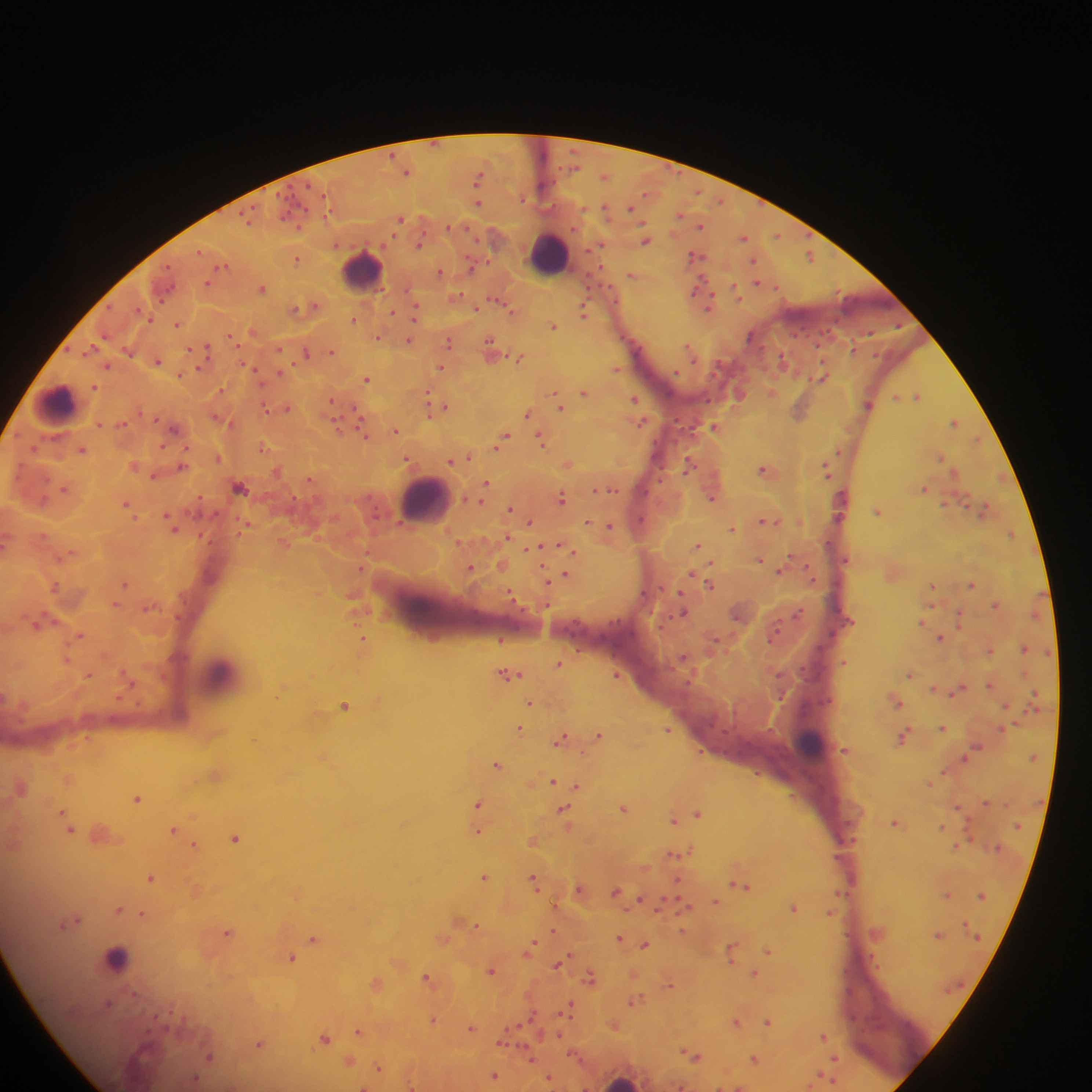
Approximate centers as [x, y] in pixels.
Summary:
  - Malaria parasite locations: [433, 143], [574, 151], [393, 153], [670, 166], [558, 167], [575, 168], [407, 171], [681, 174], [605, 176], [478, 179], [554, 179], [541, 183], [290, 186], [308, 186], [699, 192], [277, 194], [326, 197], [646, 197], [524, 201], [723, 201], [478, 202], [761, 202], [299, 204], [251, 207], [631, 208], [309, 209], [584, 209], [606, 210], [238, 213], [679, 215], [283, 216], [327, 216], [401, 218], [248, 222], [644, 223], [701, 225], [297, 226], [450, 227], [469, 228], [808, 233], [777, 235], [744, 237], [477, 238], [646, 240], [420, 243], [600, 245], [591, 252], [199, 253], [811, 255], [696, 256], [297, 259], [488, 261], [754, 261], [170, 265], [223, 266], [472, 267], [605, 267], [441, 271], [631, 275], [588, 277], [211, 281], [757, 283], [175, 285], [262, 288], [590, 288], [612, 288], [699, 291], [737, 293], [463, 295], [164, 300], [499, 300], [618, 302], [708, 305], [314, 306], [306, 307], [112, 308], [136, 308], [476, 308], [513, 310], [392, 311], [584, 311], [416, 313], [153, 319], [354, 319], [837, 322], [178, 324], [553, 326], [900, 326], [254, 331], [819, 331], [793, 333], [870, 334], [104, 336], [379, 336], [231, 337], [753, 337], [620, 338], [408, 341], [449, 341], [95, 344], [818, 347], [690, 348], [69, 349], [205, 349], [280, 349], [128, 350], [189, 350], [491, 350], [856, 350], [333, 351], [306, 352], [82, 355], [875, 355], [779, 356], [520, 358], [158, 361], [822, 361], [694, 362], [721, 363], [107, 366], [293, 366], [441, 367], [250, 368], [617, 368], [199, 369], [676, 371], [181, 374], [281, 374], [714, 374], [821, 375], [366, 379], [266, 384], [94, 385], [555, 391], [429, 392], [585, 392], [772, 392], [739, 393], [917, 396], [710, 397], [635, 398], [331, 400], [868, 404], [357, 406], [437, 406], [561, 406], [268, 408], [287, 408], [800, 410], [138, 412], [528, 414], [218, 418], [157, 419], [336, 419], [676, 420], [955, 421], [123, 423], [642, 423], [99, 424], [714, 426], [175, 428], [690, 428], [361, 429], [395, 430], [977, 438], [502, 440], [542, 440], [161, 445], [188, 445], [262, 447], [34, 450], [82, 450], [840, 451], [218, 457], [465, 457], [407, 458], [941, 458], [456, 459], [568, 463], [134, 464], [690, 464], [182, 465], [660, 469], [277, 470], [766, 470], [826, 470], [154, 476], [309, 479], [657, 480], [487, 484], [66, 487], [240, 488], [925, 488], [605, 489], [484, 490], [645, 490], [841, 492], [200, 497], [369, 497], [562, 497], [712, 497], [46, 499], [295, 499], [943, 504], [128, 505], [511, 508], [984, 509], [878, 511], [187, 512], [216, 514], [843, 516], [644, 519], [530, 521], [769, 521], [588, 522], [246, 525], [173, 526], [610, 526], [732, 529], [1012, 532], [203, 536], [507, 537], [830, 540], [6, 543], [284, 543], [459, 544], [698, 545], [537, 547], [567, 548], [573, 551], [370, 552], [66, 555], [789, 557], [760, 559], [845, 559], [711, 562], [502, 565], [471, 567], [361, 568], [781, 571], [809, 571], [693, 575], [566, 576], [548, 580], [125, 583], [971, 584], [710, 585], [933, 585], [55, 587], [661, 588], [647, 593], [682, 593], [1042, 594], [512, 595], [186, 602], [117, 603], [546, 604], [995, 604], [149, 606], [800, 608], [839, 610], [683, 611], [1035, 616], [177, 617], [610, 619], [672, 619], [960, 619], [577, 620], [739, 620], [779, 620], [850, 621], [40, 622], [622, 623], [923, 623], [662, 627], [573, 631], [780, 631], [833, 633], [81, 635], [941, 638], [363, 639], [501, 639], [769, 639], [716, 640], [581, 646], [822, 646], [1024, 648], [990, 649], [1046, 653], [613, 655], [684, 657], [66, 659], [844, 662], [559, 663], [803, 666], [782, 673], [910, 673], [1028, 673], [509, 674], [617, 674], [89, 675], [809, 679], [131, 680], [686, 684], [991, 684], [936, 689], [959, 689], [1035, 693], [781, 698], [122, 699], [831, 699], [897, 701], [822, 702], [1030, 702], [530, 703], [139, 705], [345, 705], [809, 705], [735, 712], [1013, 722], [943, 727], [520, 728], [999, 728], [668, 729], [769, 729], [723, 731], [600, 734], [904, 735], [561, 738], [750, 742], [979, 747], [845, 749], [701, 750], [965, 757], [1033, 757], [498, 764], [942, 771], [216, 774], [756, 774], [69, 778], [555, 781], [931, 782], [566, 783], [578, 786], [21, 787], [793, 796], [137, 798], [986, 802], [479, 804], [959, 807], [624, 808], [564, 811], [698, 812], [675, 820], [68, 821], [850, 821], [897, 822], [1020, 825], [942, 826], [71, 829], [176, 829], [479, 830], [967, 830], [102, 834], [236, 837], [842, 838], [533, 840], [856, 840], [971, 840], [196, 845], [958, 845], [999, 848], [678, 853], [838, 855], [486, 876], [151, 877], [535, 879], [678, 880], [741, 885], [581, 888], [196, 889], [617, 891], [849, 893], [947, 894], [662, 895], [982, 895], [641, 898], [716, 901], [684, 907], [793, 907], [120, 909], [628, 911], [829, 912], [143, 913], [659, 913], [73, 921], [477, 926], [963, 926], [553, 930], [682, 931], [229, 932], [938, 935], [314, 937], [977, 937], [443, 938], [621, 938], [645, 944], [531, 948], [768, 950], [732, 951], [293, 958], [558, 963], [491, 969], [754, 973], [591, 976], [428, 978], [377, 982], [670, 982], [963, 982], [636, 1001], [111, 1003], [537, 1009], [569, 1010], [171, 1012], [156, 1014], [434, 1019], [529, 1019], [737, 1021], [768, 1021], [520, 1024], [614, 1024], [472, 1026], [542, 1029], [147, 1030], [359, 1031], [559, 1034], [824, 1035], [325, 1038], [503, 1040], [259, 1044], [571, 1054], [694, 1055], [209, 1057], [530, 1057], [835, 1058], [754, 1059], [581, 1060], [350, 1061], [379, 1067], [833, 1071], [495, 1075], [550, 1077], [829, 1077], [194, 1081], [411, 1085], [680, 1085], [363, 1086]
  - Leukocyte locations: [549, 254], [361, 270], [56, 403], [425, 498], [222, 675], [810, 744], [115, 958], [887, 1011], [622, 1081]
  - Preparation: thick blood smear
  - Field of view: single
  - Capture: mobile-phone photograph through a microscope
  - Country: Ghana
  - Image size: 1092×1092 pixels